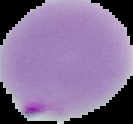
preparation = thin blood film
result = malaria parasites identified
image size = 133×124 pixels
image type = segmented cell region with the area outside set to black